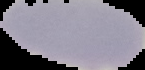
Summary:
  - Preparation: thin blood film
  - Image size: 145×70 pixels
  - Image type: cell region segmented out of the field of view; surrounding area masked to black
  - Result: no Plasmodium parasites seen